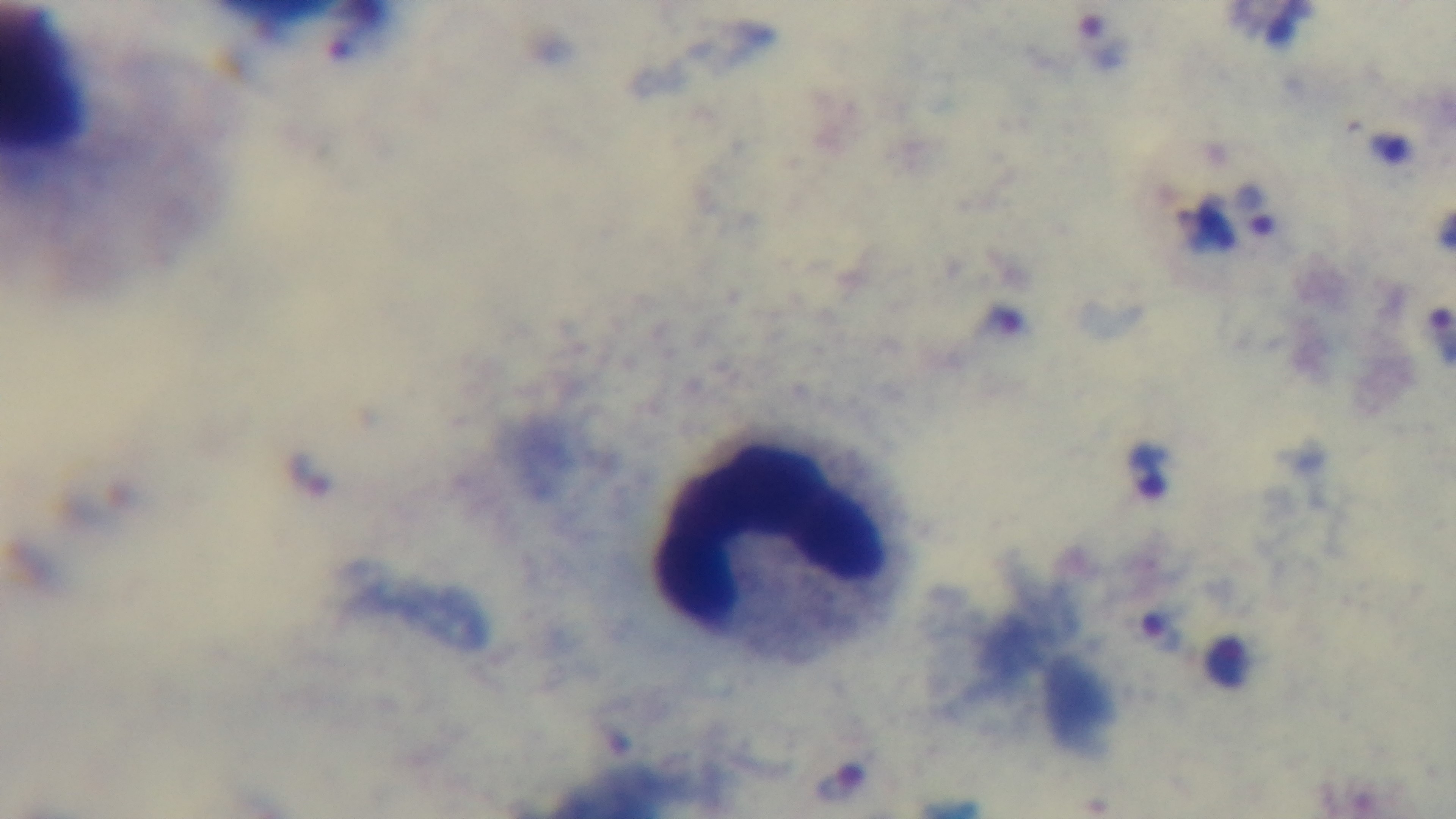
Summary:
  - Malaria status: positive
  - Objective: 100x oil immersion
  - Capture: mounted 4K digital camera
  - Modality: light microscopy
  - Field of view: one from the slide
  - Stain: Giemsa
  - Preparation: thick